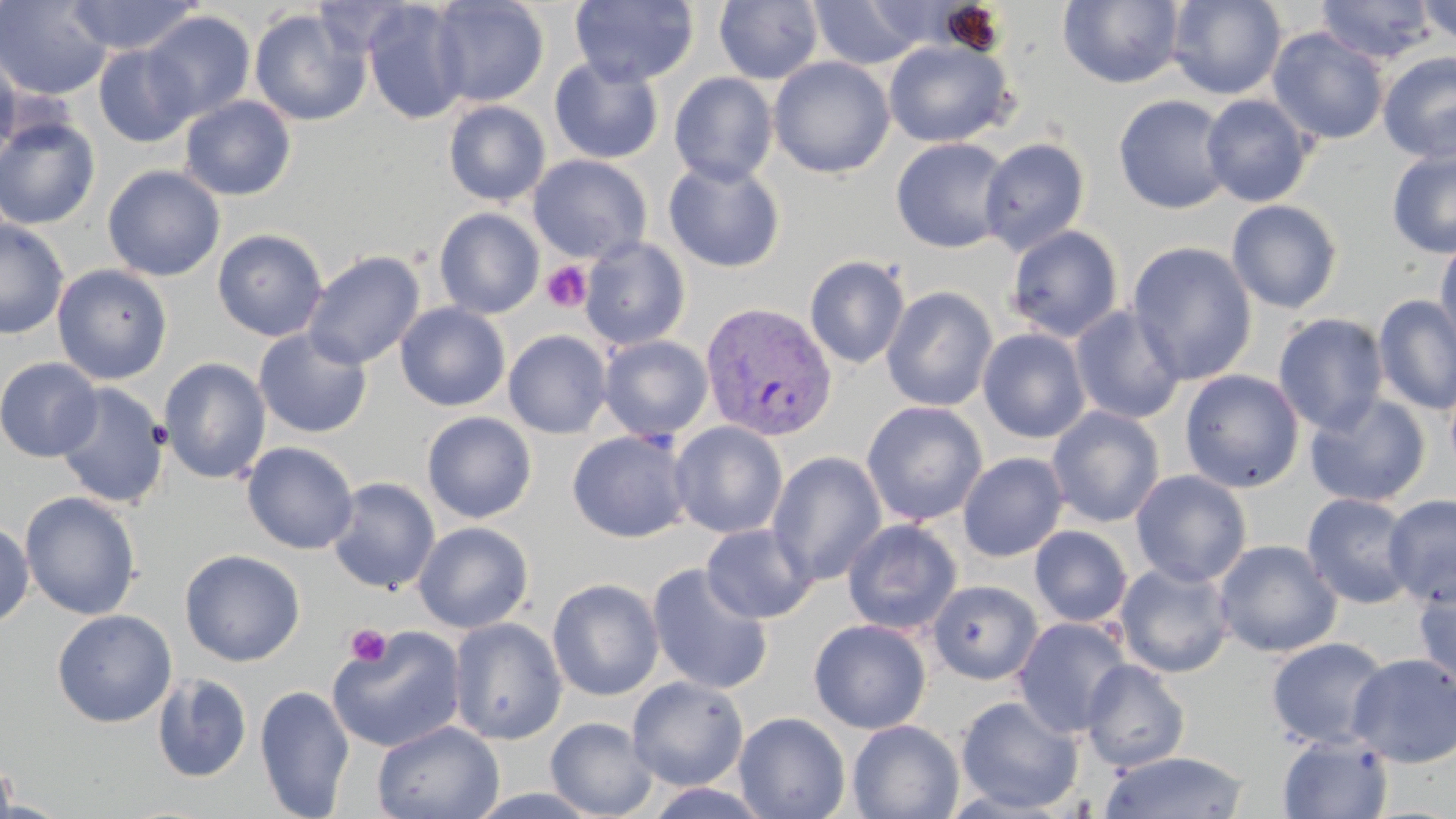

Summary:
  - Coordinate format: approximate bounding boxes as (x1, y1, x2, y2) in pixels
  - Uninfected red blood cell locations: (0, 0, 114, 100), (65, 0, 203, 55), (429, 0, 550, 108), (569, 0, 700, 88), (1057, 0, 1186, 89), (1167, 0, 1287, 100), (1314, 0, 1438, 65), (1415, 0, 1456, 46), (713, 1, 824, 85), (808, 1, 932, 70), (362, 2, 471, 124), (249, 8, 370, 126), (141, 10, 256, 122), (1267, 27, 1389, 145), (883, 40, 1014, 148), (93, 44, 197, 147), (0, 48, 20, 166), (1378, 51, 1456, 163), (549, 56, 663, 164), (768, 56, 895, 179), (668, 72, 779, 187), (1113, 94, 1233, 214), (1200, 94, 1314, 207), (179, 95, 296, 201), (443, 100, 551, 206), (0, 116, 101, 230), (891, 137, 1013, 253), (979, 138, 1091, 255), (1386, 148, 1456, 259), (528, 154, 652, 263), (662, 158, 786, 272), (102, 164, 225, 282), (1226, 200, 1343, 314), (434, 206, 544, 319), (0, 219, 69, 340), (1004, 225, 1124, 342), (212, 229, 329, 341), (1434, 235, 1456, 354), (579, 236, 691, 350), (1127, 241, 1258, 385), (303, 250, 425, 371), (804, 255, 910, 370), (52, 264, 173, 385), (881, 286, 998, 412), (1373, 295, 1455, 415), (395, 302, 511, 412), (1069, 305, 1187, 424), (1272, 313, 1389, 435), (978, 328, 1091, 443), (253, 329, 373, 439), (503, 330, 612, 438), (598, 335, 713, 441), (0, 357, 103, 462), (158, 357, 271, 484), (1179, 369, 1305, 493), (53, 382, 170, 509), (1304, 393, 1431, 507), (861, 400, 988, 527), (1046, 405, 1165, 527), (422, 411, 537, 524), (669, 421, 789, 539), (567, 430, 692, 542), (242, 442, 358, 554), (767, 451, 887, 586), (958, 452, 1069, 562), (1130, 469, 1252, 587), (327, 476, 441, 594), (20, 491, 142, 620), (1301, 493, 1418, 609), (1384, 493, 1456, 608), (842, 518, 963, 635), (0, 520, 34, 628), (413, 521, 534, 633), (701, 523, 818, 624), (1030, 525, 1133, 627), (1213, 539, 1343, 657), (179, 549, 305, 667), (1113, 561, 1236, 678), (646, 562, 774, 695), (1413, 574, 1456, 692), (547, 577, 665, 701), (927, 579, 1044, 685), (52, 609, 176, 727), (1012, 616, 1134, 738), (449, 617, 567, 745), (809, 619, 931, 734), (326, 627, 467, 752), (1266, 637, 1391, 749), (1347, 653, 1456, 768), (1080, 659, 1190, 772), (151, 672, 252, 783), (627, 676, 748, 791), (254, 684, 355, 818), (955, 695, 1084, 815), (733, 711, 851, 819), (545, 716, 657, 819), (847, 719, 964, 819), (371, 720, 505, 819), (1276, 733, 1394, 818), (1099, 751, 1251, 819), (0, 754, 18, 819), (642, 783, 777, 819)
  - Platelet locations: (541, 260, 593, 313), (344, 623, 393, 668)
  - Plasmodium vivax-infected red blood cell locations: (700, 302, 837, 443)
  - Slide-level diagnosis: Plasmodium vivax
  - Magnification: 1000x
  - Image size: 1456×819 pixels
  - Field of view: one of a larger specimen
  - Modality: optical microscopy
  - Preparation: thin blood film
  - Stain: May-Grünwald-Giemsa